Report the malaria status of this cell.
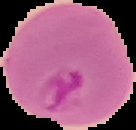

It is parasitized.

Summary:
  - Image size: 136×130 pixels
  - Preparation: thin blood film
  - Image type: segmented cell region on a black background